Name the parasite shown.
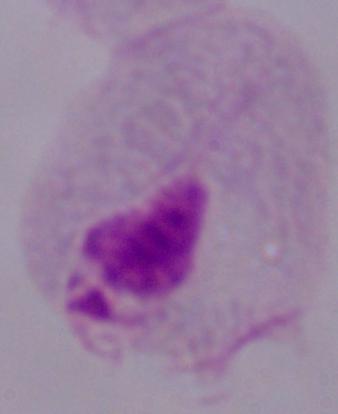

This is a trichomonad.

modality = photomicrograph
magnification = 1000x